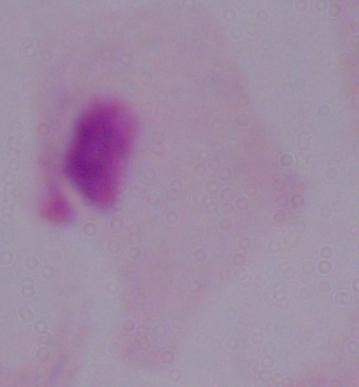

Summary:
  - Modality: micrograph
  - Identification: trichomonad
  - Magnification: 1000x